Classify this cell by malaria status.
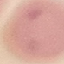

Uninfected.

Acquired by smartphone through the microscope eyepiece. Cell patch, automatically extracted from a larger field of view and resized to 64 × 64 pixels. Giemsa stain. Thin blood smear.